Identify the parasite.
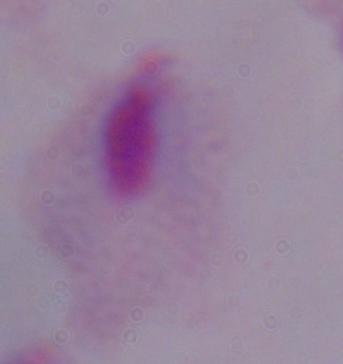
A trichomonad.

modality = photomicrograph
magnification = 1000x